Describe the morphology of the red blood cells.
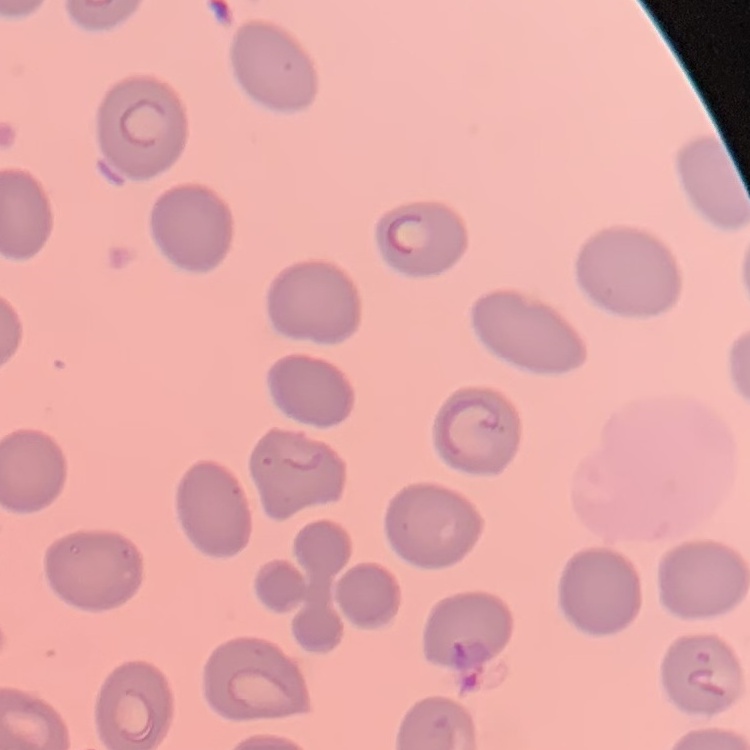

No rouleaux formation.

stain = Field's or Giemsa
preparation = thin peripheral smear
image type = one tile cut from a larger photomicrograph